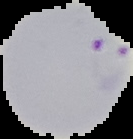
{
  "image_size": "133×139 pixels",
  "preparation": "thin blood film",
  "image_type": "segmented cell region with the area outside set to black",
  "malaria_status": "parasitized"
}